Assess this cell for malaria.
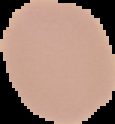

It is uninfected.

Summary:
  - Image type: segmented cell region on a black background
  - Preparation: thin blood smear
  - Image size: 115×124 pixels